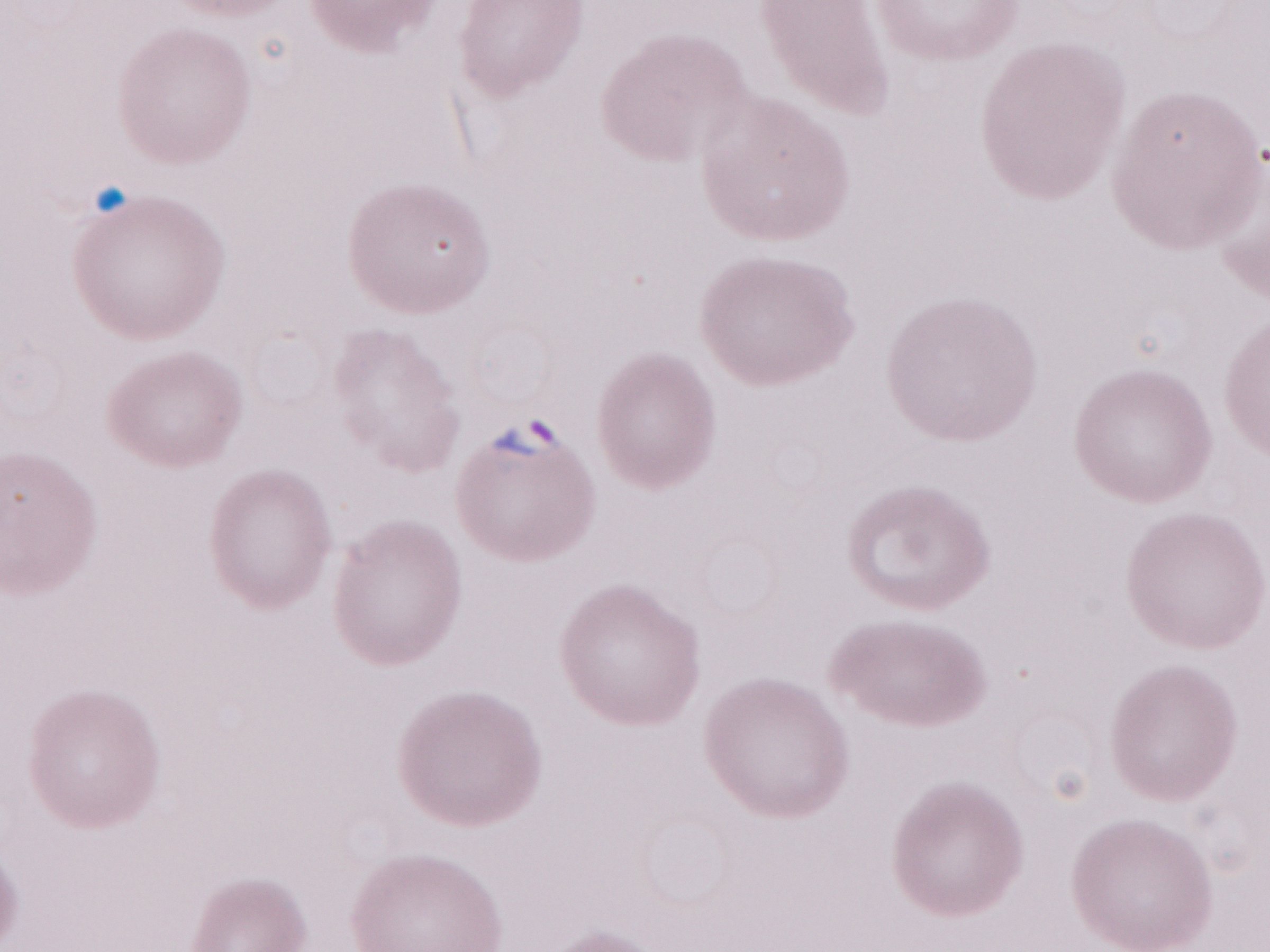 Malaria diagnosis (patient-level): positive. Olympus BX43 microscope and DP73 digital camera. Magnification: 1,000x. May-Grünwald-Giemsa-stained preparation. Image is 1270×952 pixels. Thin blood film. One field of this slide.